Give the position of every leukocyte visible.
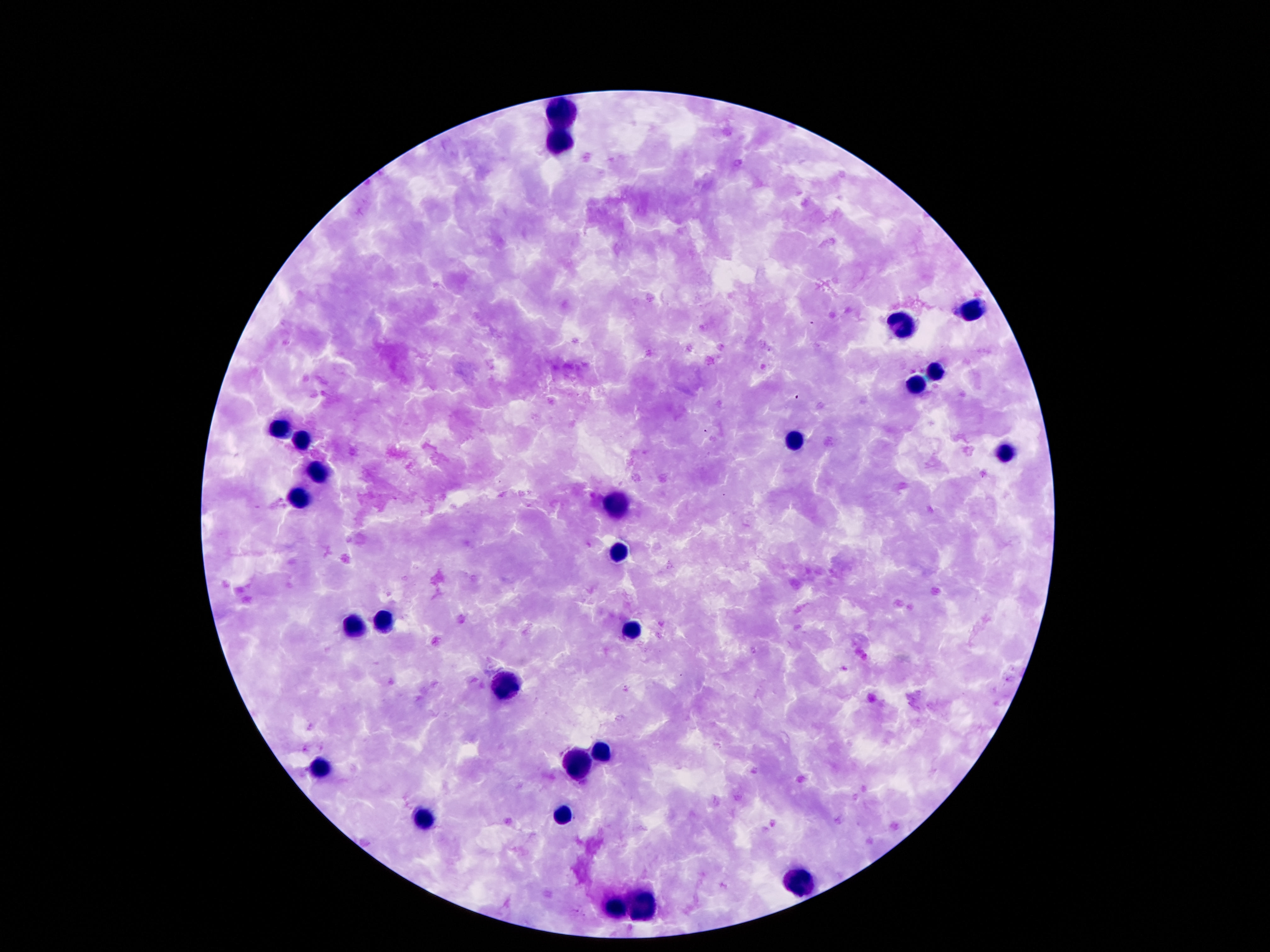
Approximate centers as {x, y} in pixels.
Leukocytes: {568, 115}, {557, 140}, {975, 309}, {899, 324}, {934, 373}, {918, 383}, {281, 427}, {789, 439}, {303, 442}, {1006, 453}, {320, 471}, {299, 500}, {619, 506}, {621, 553}, {385, 620}, {354, 627}, {631, 629}, {506, 685}, {600, 749}, {580, 761}, {318, 770}, {561, 815}, {424, 819}, {799, 881}, {643, 903}, {619, 909}.

Summary:
  - Stain: Giemsa
  - Preparation: thick blood smear
  - Field of view: one from this slide
  - Image size: 1270×952 pixels
  - Patient malaria status: negative
  - Capture: smartphone camera through the microscope eyepiece
  - Magnification: 100x